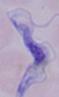
{
  "identification": "trypanosome",
  "modality": "photomicrograph",
  "magnification": "1000x"
}